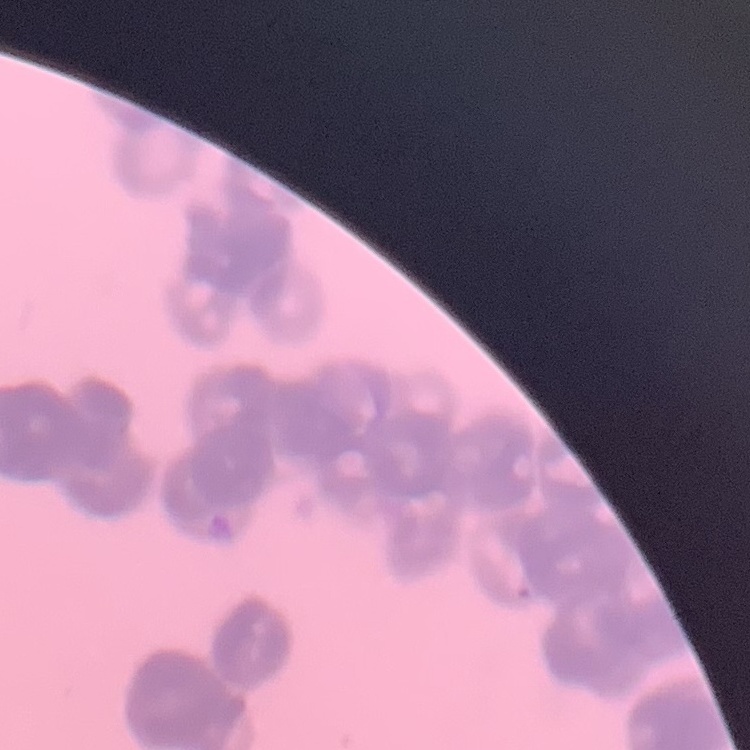 The red blood cells exhibit rouleaux formation. Field's or Giemsa stain. One tile cut from a larger photomicrograph. Thin peripheral smear.